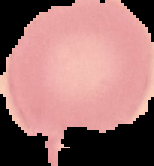
Summary:
  - Result: no malaria parasites detected
  - Preparation: thin blood film
  - Image size: 154×166 pixels
  - Image type: cell region segmented out of the field of view; surrounding area masked to black